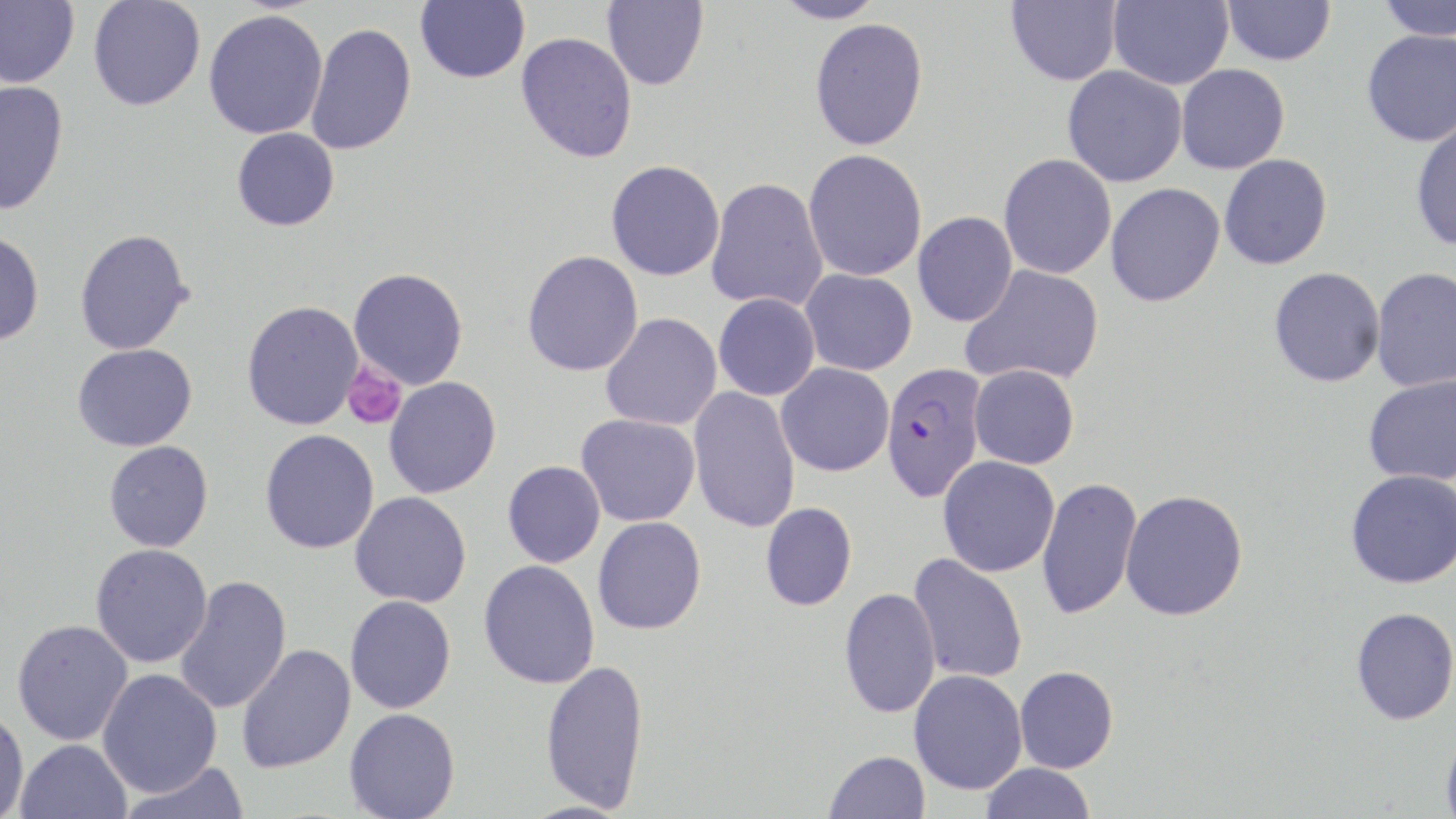
slide-level diagnosis = Plasmodium falciparum
platelet locations = approximate bounding boxes as (x1, y1, x2, y2) in pixels: (342, 364, 406, 430)
uninfected red blood cell locations = approximate bounding boxes as (x1, y1, x2, y2) in pixels: (0, 0, 79, 89), (87, 0, 206, 112), (415, 0, 529, 83), (601, 0, 709, 90), (771, 0, 887, 24), (1005, 0, 1122, 86), (1108, 0, 1233, 90), (1222, 0, 1335, 66), (1376, 0, 1456, 40), (203, 9, 328, 140), (809, 18, 928, 151), (305, 22, 417, 156), (1361, 29, 1456, 147), (516, 31, 638, 163), (1176, 64, 1289, 174), (1062, 66, 1187, 187), (0, 81, 69, 215), (1410, 118, 1456, 252), (231, 128, 339, 231), (803, 149, 927, 281), (998, 153, 1116, 279), (1219, 154, 1333, 270), (606, 160, 725, 281), (706, 177, 828, 312), (1105, 183, 1226, 307), (913, 211, 1017, 327), (74, 228, 193, 355), (0, 229, 44, 347), (521, 250, 644, 376), (960, 264, 1105, 387), (1268, 267, 1385, 387), (1370, 267, 1456, 392), (348, 268, 469, 389), (800, 269, 917, 375), (713, 293, 820, 401), (242, 300, 364, 430), (600, 314, 722, 431), (73, 343, 197, 451), (776, 362, 894, 477), (969, 364, 1080, 469), (1362, 375, 1456, 485), (384, 377, 501, 498), (687, 386, 801, 533), (576, 414, 700, 527), (260, 429, 379, 554), (103, 441, 214, 552), (938, 456, 1059, 577), (502, 461, 606, 568), (1345, 469, 1456, 589), (1037, 476, 1142, 620), (1120, 489, 1249, 621), (350, 491, 472, 608), (760, 502, 857, 611), (592, 516, 707, 635), (90, 543, 213, 668), (908, 553, 1028, 683), (478, 560, 600, 689), (173, 575, 292, 715), (839, 586, 941, 719), (345, 595, 457, 714), (1350, 607, 1456, 725), (11, 619, 134, 746), (236, 643, 356, 773), (540, 659, 650, 812), (1014, 666, 1119, 773), (97, 668, 222, 798), (909, 669, 1027, 794), (344, 708, 460, 819), (0, 709, 29, 819), (1440, 730, 1456, 819), (15, 738, 132, 819), (824, 750, 931, 819), (119, 762, 252, 819), (980, 763, 1096, 819)
stain = May-Grünwald-Giemsa
field of view = single
preparation = thin blood film
Plasmodium falciparum-infected red blood cell locations = approximate bounding boxes as (x1, y1, x2, y2) in pixels: (880, 362, 987, 503)
modality = optical microscopy
magnification = 1000x
image size = 1456×819 pixels